Report the malaria status of this cell.
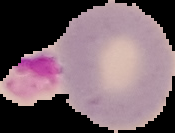

It is uninfected.

Summary:
  - Image type: segmented cell region on a black background
  - Image size: 175×133 pixels
  - Preparation: thin blood film